Report the malaria status of this cell.
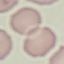
Uninfected.

Giemsa-stained preparation. Thin smear of blood. Automatically extracted cell patch, resized to 64 × 64 pixels. Photographed with a smartphone camera at the microscope eyepiece.